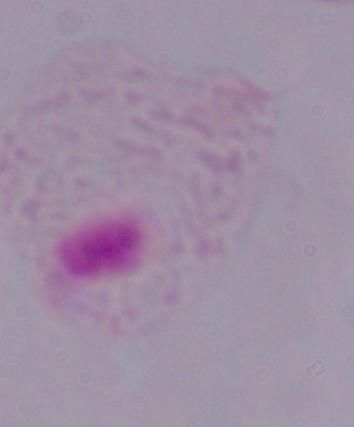 Captured at 1000x magnification. A trichomonad is seen. Micrograph.